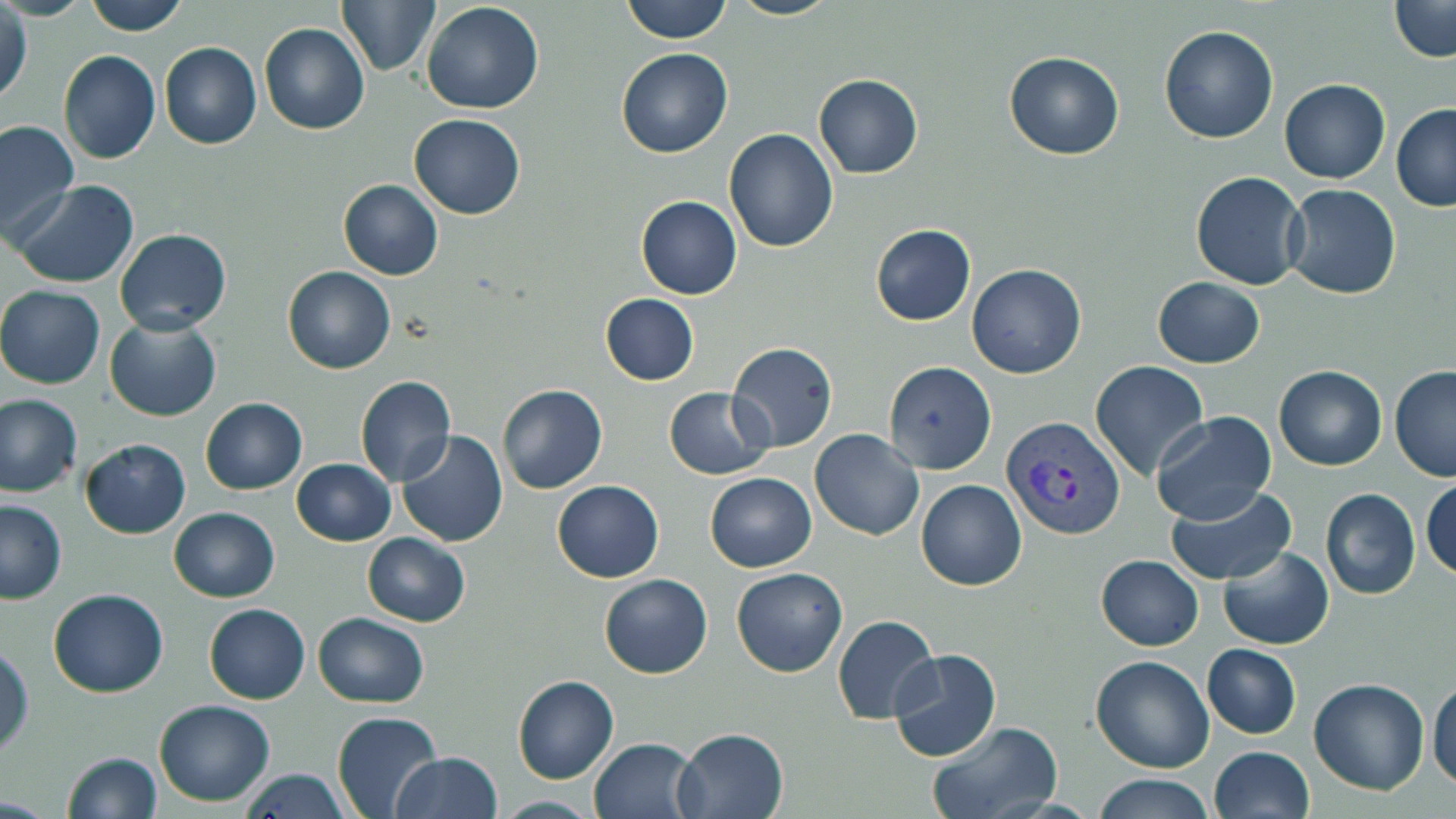
slide-level diagnosis = Plasmodium vivax
preparation = thin blood film
modality = light microscopy
field of view = one of a larger specimen
uninfected red blood cell locations = approximate bounding boxes as named x1/y1/x2/y2 corners in pixels: (x1=84, y1=0, x2=189, y2=35), (x1=336, y1=0, x2=439, y2=77), (x1=621, y1=0, x2=731, y2=44), (x1=728, y1=0, x2=840, y2=20), (x1=1388, y1=0, x2=1455, y2=62), (x1=421, y1=2, x2=546, y2=114), (x1=0, y1=5, x2=31, y2=108), (x1=259, y1=23, x2=370, y2=135), (x1=1159, y1=25, x2=1278, y2=143), (x1=159, y1=42, x2=262, y2=150), (x1=616, y1=48, x2=734, y2=160), (x1=59, y1=50, x2=161, y2=164), (x1=1005, y1=53, x2=1124, y2=159), (x1=813, y1=73, x2=923, y2=178), (x1=1278, y1=80, x2=1390, y2=183), (x1=1391, y1=104, x2=1456, y2=212), (x1=409, y1=113, x2=526, y2=219), (x1=0, y1=120, x2=79, y2=240), (x1=724, y1=129, x2=839, y2=252), (x1=1191, y1=171, x2=1307, y2=290), (x1=9, y1=179, x2=140, y2=289), (x1=338, y1=179, x2=444, y2=281), (x1=1283, y1=185, x2=1401, y2=299), (x1=636, y1=195, x2=742, y2=299), (x1=871, y1=224, x2=976, y2=326), (x1=115, y1=228, x2=232, y2=334), (x1=967, y1=264, x2=1086, y2=378), (x1=282, y1=267, x2=395, y2=374), (x1=1152, y1=277, x2=1265, y2=368), (x1=0, y1=285, x2=105, y2=389), (x1=600, y1=294, x2=698, y2=386), (x1=105, y1=317, x2=221, y2=422), (x1=725, y1=343, x2=839, y2=452), (x1=882, y1=361, x2=996, y2=474), (x1=1091, y1=361, x2=1209, y2=479), (x1=1390, y1=364, x2=1456, y2=483), (x1=1274, y1=365, x2=1387, y2=471), (x1=355, y1=376, x2=455, y2=487), (x1=498, y1=383, x2=607, y2=494), (x1=664, y1=386, x2=772, y2=479), (x1=0, y1=394, x2=82, y2=497), (x1=200, y1=397, x2=307, y2=494), (x1=1151, y1=411, x2=1277, y2=525), (x1=810, y1=429, x2=924, y2=540), (x1=396, y1=430, x2=508, y2=547), (x1=79, y1=438, x2=191, y2=539), (x1=292, y1=458, x2=395, y2=546), (x1=704, y1=471, x2=817, y2=572), (x1=1421, y1=476, x2=1455, y2=583), (x1=916, y1=479, x2=1027, y2=591), (x1=551, y1=480, x2=665, y2=583), (x1=1167, y1=484, x2=1295, y2=583), (x1=1320, y1=487, x2=1421, y2=600), (x1=0, y1=498, x2=67, y2=604), (x1=169, y1=506, x2=279, y2=602), (x1=362, y1=533, x2=470, y2=626), (x1=1219, y1=546, x2=1333, y2=649), (x1=1096, y1=555, x2=1203, y2=650), (x1=731, y1=567, x2=848, y2=677), (x1=599, y1=574, x2=712, y2=679), (x1=46, y1=588, x2=169, y2=697), (x1=204, y1=603, x2=311, y2=704), (x1=312, y1=612, x2=429, y2=707), (x1=832, y1=615, x2=939, y2=724), (x1=1202, y1=644, x2=1301, y2=740), (x1=0, y1=645, x2=34, y2=759), (x1=888, y1=648, x2=1002, y2=762), (x1=1091, y1=655, x2=1215, y2=773), (x1=1428, y1=672, x2=1456, y2=791), (x1=513, y1=676, x2=619, y2=786), (x1=1308, y1=678, x2=1429, y2=796), (x1=154, y1=699, x2=275, y2=805), (x1=332, y1=712, x2=443, y2=819), (x1=925, y1=720, x2=1064, y2=819), (x1=676, y1=727, x2=789, y2=819), (x1=589, y1=737, x2=703, y2=819), (x1=1209, y1=746, x2=1314, y2=819), (x1=62, y1=752, x2=162, y2=819), (x1=391, y1=752, x2=503, y2=818), (x1=237, y1=767, x2=351, y2=819), (x1=1092, y1=774, x2=1215, y2=819), (x1=495, y1=795, x2=599, y2=817)
Plasmodium vivax-infected red blood cell locations = approximate bounding boxes as named x1/y1/x2/y2 corners in pixels: (x1=1003, y1=414, x2=1126, y2=539)
stain = May-Grünwald-Giemsa
magnification = 1000x
image size = 1456×819 pixels